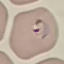 Malaria status: parasitized. Giemsa-stained preparation. Thin blood film. Automatically extracted cell patch, resized to 64 × 64 pixels. Photographed with a smartphone camera at the microscope eyepiece.